Outline each uninfected red blood cell.
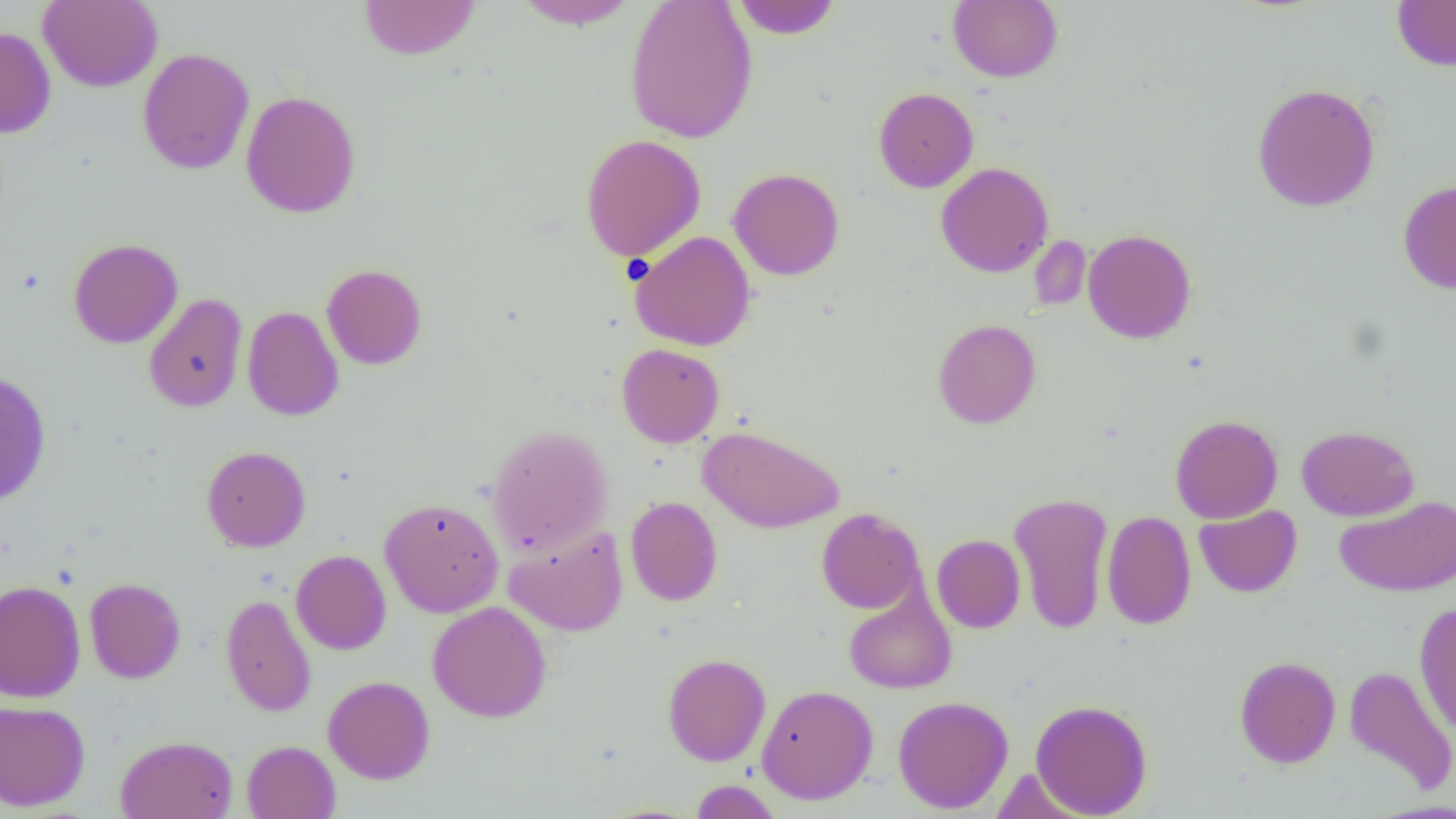

Approximate bounding boxes as [x1, y1, x2, y2] in pixels.
Uninfected red blood cells: [39, 0, 162, 91], [358, 0, 480, 60], [513, 0, 640, 30], [624, 0, 758, 145], [731, 0, 842, 39], [1392, 0, 1456, 70], [948, 1, 1063, 83], [0, 26, 57, 138], [137, 48, 254, 174], [1251, 82, 1381, 212], [873, 87, 979, 193], [240, 90, 361, 218], [580, 134, 706, 261], [935, 162, 1053, 278], [728, 167, 845, 281], [1397, 180, 1456, 294], [1082, 228, 1197, 344], [629, 231, 756, 351], [1028, 235, 1092, 313], [68, 237, 183, 349], [321, 263, 428, 370], [144, 293, 248, 413], [242, 305, 344, 421], [932, 318, 1041, 429], [616, 343, 724, 448], [0, 371, 52, 506], [1170, 414, 1283, 523], [486, 424, 613, 556], [698, 425, 845, 533], [1296, 425, 1420, 521], [201, 446, 311, 552], [1008, 491, 1114, 634], [1335, 494, 1456, 596], [626, 496, 723, 606], [378, 497, 504, 617], [1193, 504, 1302, 598], [816, 508, 924, 613], [1101, 510, 1196, 630], [504, 524, 629, 637], [931, 534, 1026, 633], [291, 550, 391, 655], [84, 577, 186, 683], [0, 580, 86, 703], [843, 586, 956, 694], [221, 593, 316, 717], [427, 601, 552, 722], [1414, 602, 1456, 735], [662, 653, 771, 766], [1234, 655, 1340, 768], [1343, 664, 1456, 796], [323, 675, 435, 784], [756, 684, 878, 804], [892, 696, 1013, 813], [1030, 698, 1153, 817], [0, 699, 90, 810], [115, 735, 238, 818], [242, 740, 340, 818], [689, 779, 782, 819].

slide_level_diagnosis: no evidence of blood parasites
field_of_view: single
modality: optical microscopy
preparation: thin blood smear
image_size: 1456×819 pixels
magnification: 1000x